Comment on the morphology of the erythrocytes.
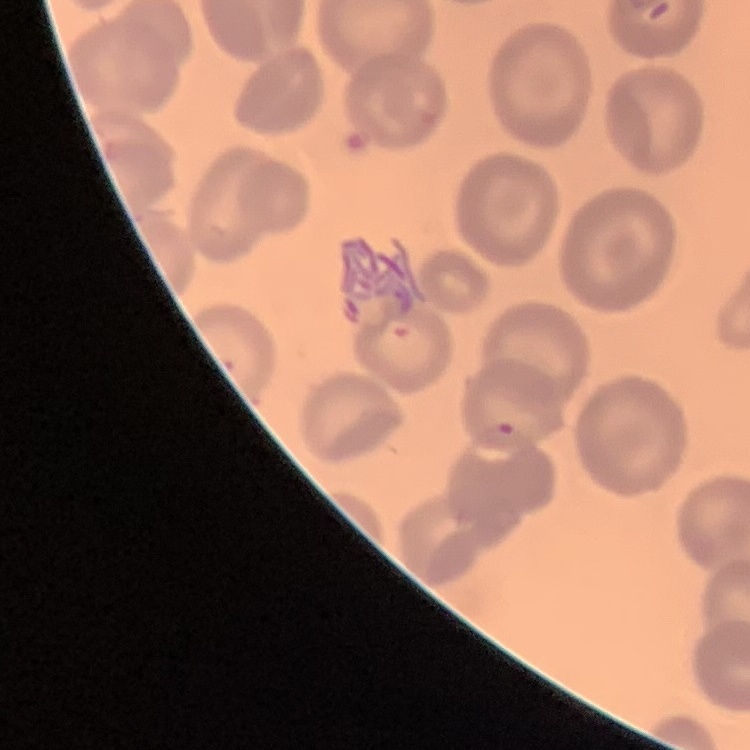

They show no rouleaux formation.

Stained with either Field's or Giemsa. Square crop of a larger photomicrograph. Thin blood smear.